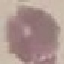

Summary:
  - Malaria status: uninfected
  - Capture: smartphone through the microscope eyepiece
  - Image type: cell patch, automatically extracted from a larger field of view and resized to 64 × 64 pixels
  - Stain: Giemsa
  - Preparation: thin blood film